Comment on the morphology of the red blood cells.
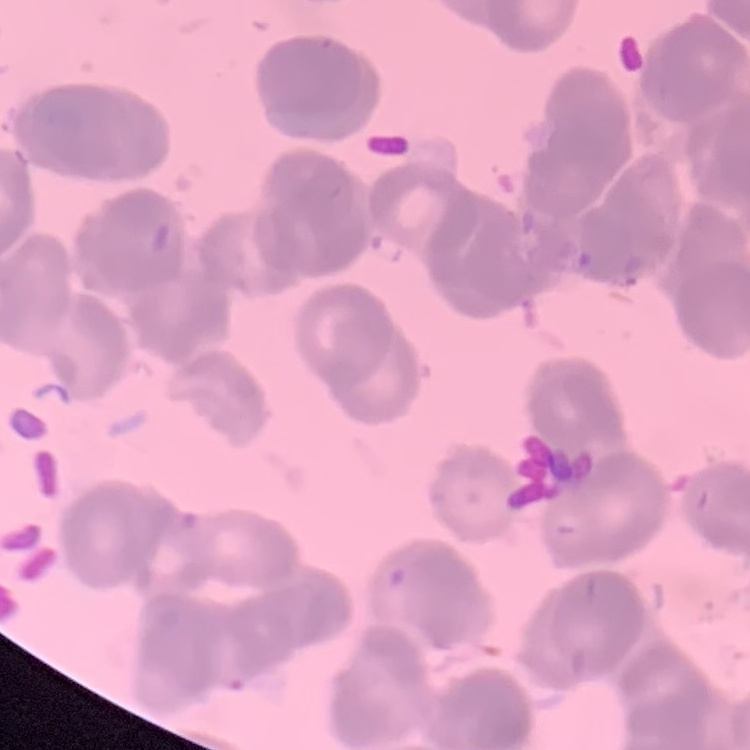

Rouleaux formation.

Square crop of a larger photomicrograph. Field's or Giemsa stain. Thin peripheral smear.